Classify this cell by malaria status.
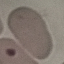
Uninfected.

Summary:
  - Stain: Giemsa
  - Capture: smartphone camera at the microscope eyepiece
  - Image type: cell patch, automatically extracted from a larger field of view and resized to 64 × 64 pixels
  - Preparation: thin blood film